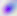
Toxoplasma gondii is shown. Captured at 400x magnification. Micrograph.